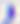 400x magnification. Toxoplasma gondii is shown. Photomicrograph.